Give the position of every malaria parasite.
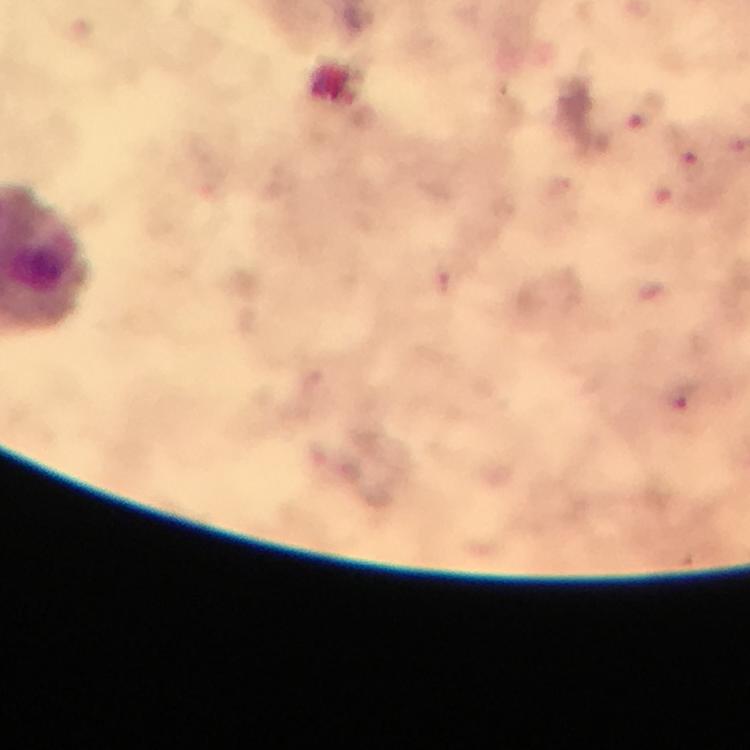

Approximate centers as [x, y] in pixels.
Malaria parasites: [644, 115], [692, 163], [685, 399].

Photographed with a smartphone mounted on the microscope. Cropped region of a single field of view. From a malaria diagnostic workup. Giemsa stain. Immersion oil applied. Image is 750×750 pixels. Thick blood film. At 100x magnification.